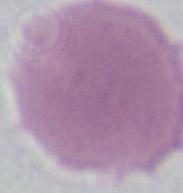
identification = erythrocyte
modality = photomicrograph
magnification = 1000x